Assess this cell for malaria.
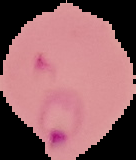

Parasitized.

image size = 136×160 pixels
preparation = thin blood smear
image type = cell region segmented out of the field of view; surrounding area masked to black